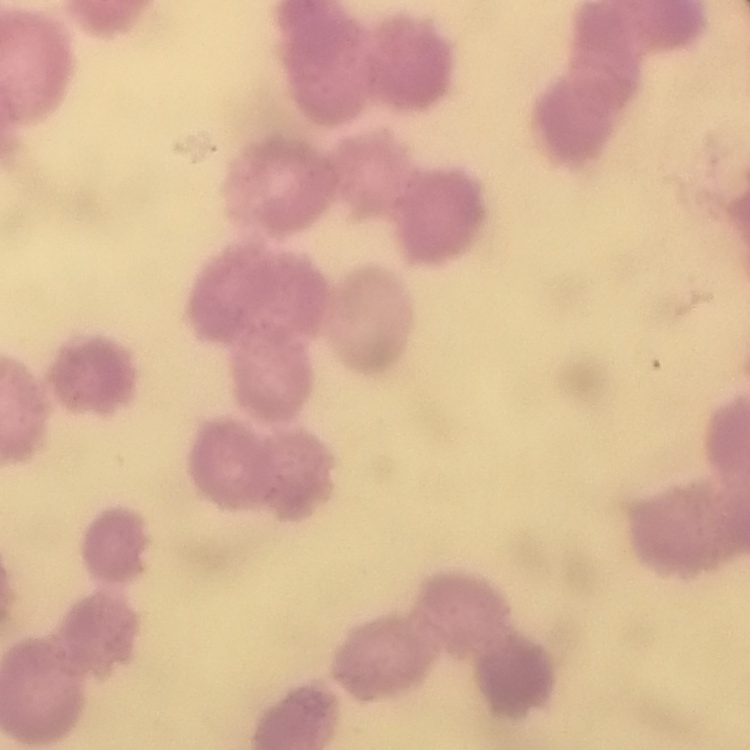

Summary:
  - Red blood cell morphology: rouleaux formation
  - Preparation: thin peripheral smear
  - Stain: Field's or Giemsa
  - Image type: square crop of a larger photomicrograph